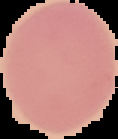
{
  "result": "no malaria parasites seen",
  "preparation": "thin blood film",
  "image_type": "cell region segmented out of the field of view; surrounding area masked to black",
  "image_size": "118×139 pixels"
}